Assess the morphology of the erythrocytes.
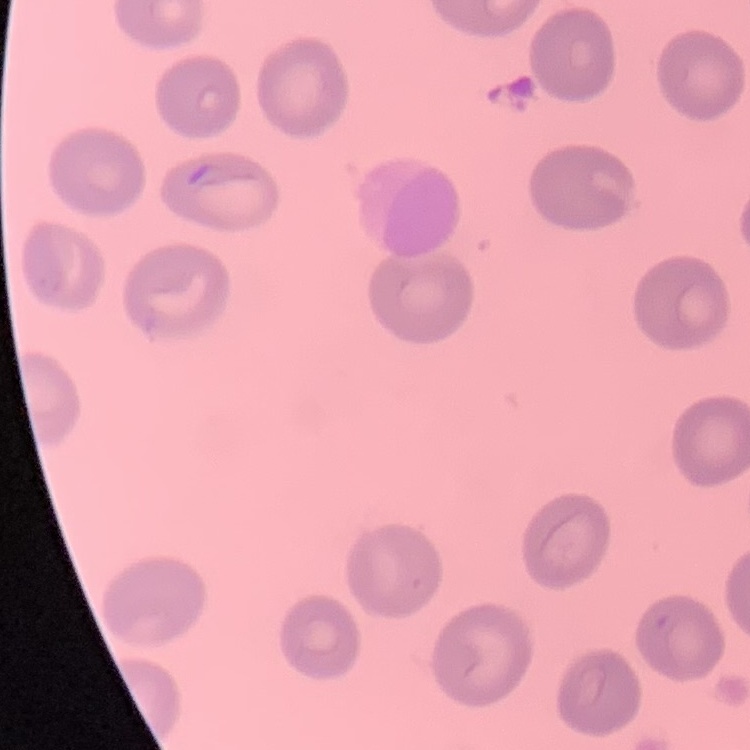

No rouleaux formation.

Stained with either Field's or Giemsa. Thin peripheral smear. One tile cut from a larger photomicrograph.